Name the blood parasite species.
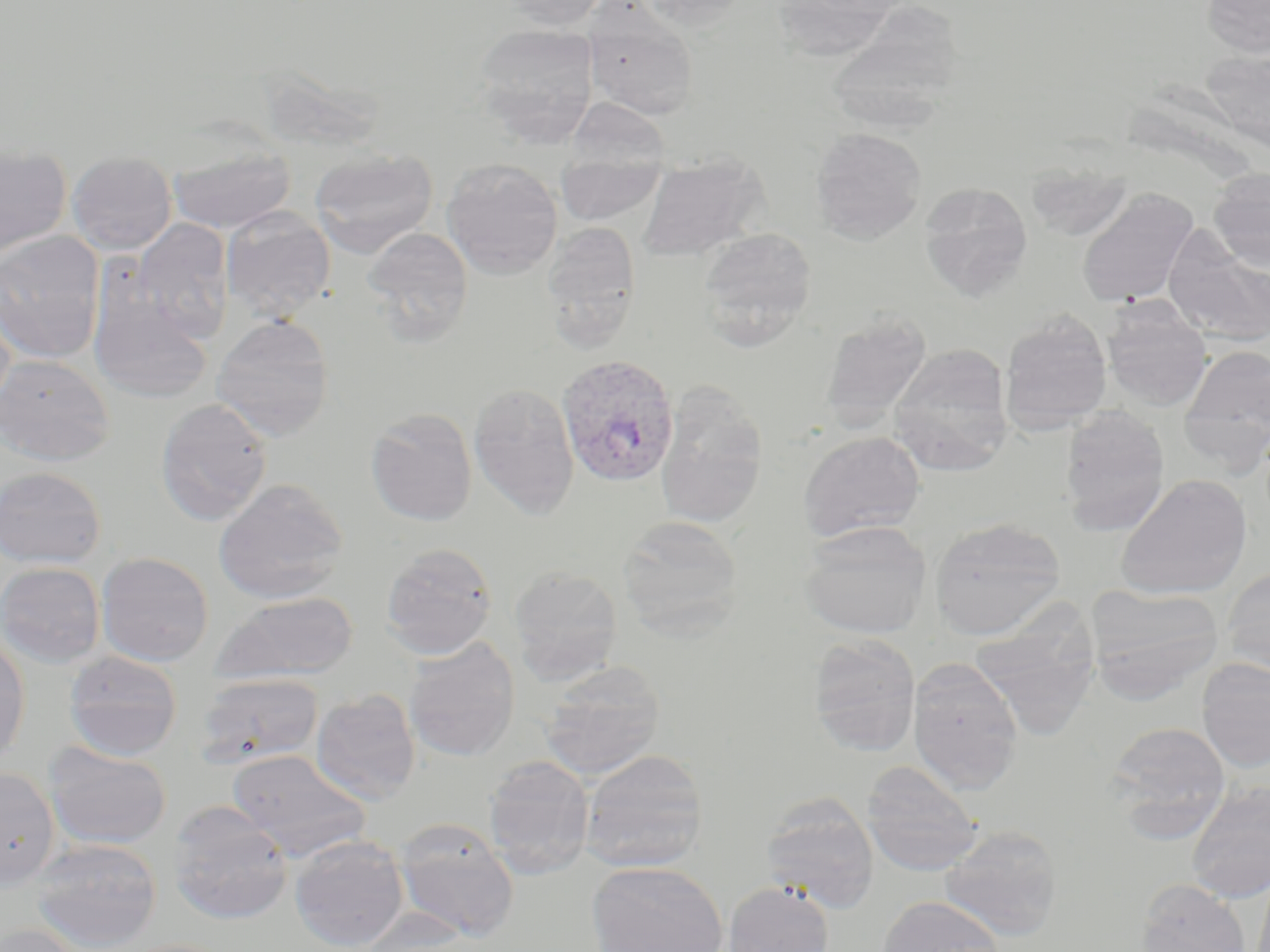
Plasmodium vivax.

Summary:
  - Coordinate format: approximate bounding boxes as (x1, y1, x2, y2) in pixels
  - Plasmodium vivax-infected red blood cell locations: (556, 354, 681, 488)
  - Uninfected red blood cell locations: (496, 0, 612, 30), (636, 0, 751, 29), (776, 0, 901, 63), (1200, 0, 1270, 58), (836, 2, 964, 138), (582, 5, 701, 121), (472, 22, 600, 146), (1200, 48, 1270, 153), (565, 97, 671, 172), (810, 127, 927, 244), (0, 142, 72, 260), (167, 144, 295, 233), (310, 147, 438, 257), (66, 151, 178, 255), (636, 153, 769, 263), (441, 157, 563, 279), (555, 159, 668, 226), (1025, 165, 1134, 241), (1208, 168, 1270, 273), (918, 182, 1034, 303), (1076, 188, 1200, 308), (221, 207, 336, 320), (132, 218, 234, 341), (541, 220, 642, 353), (1162, 226, 1270, 348), (361, 227, 473, 344), (696, 227, 817, 347), (0, 230, 105, 364), (87, 285, 213, 405), (1101, 298, 1213, 411), (0, 306, 15, 414), (819, 310, 932, 433), (999, 311, 1113, 434), (211, 314, 334, 441), (888, 344, 1014, 475), (1178, 345, 1270, 472), (0, 354, 114, 464), (468, 381, 580, 519), (654, 383, 769, 528), (155, 397, 273, 526), (1059, 405, 1171, 536), (365, 407, 478, 526), (797, 431, 926, 543), (0, 466, 107, 569), (1115, 473, 1253, 600), (213, 478, 348, 604), (617, 515, 743, 637), (928, 516, 1066, 641), (799, 520, 932, 639), (380, 542, 498, 659), (96, 551, 214, 666), (1, 561, 105, 668), (509, 565, 623, 684), (1221, 567, 1270, 677), (1085, 584, 1223, 703), (214, 592, 359, 684), (970, 608, 1100, 740), (0, 630, 30, 765), (807, 633, 921, 757), (403, 637, 520, 763), (63, 650, 183, 760), (907, 657, 1024, 794), (1196, 659, 1270, 773), (539, 661, 665, 780), (194, 673, 324, 768), (310, 689, 421, 806), (1106, 721, 1231, 836), (43, 742, 172, 849), (227, 749, 372, 861), (579, 749, 709, 873), (483, 755, 595, 879), (860, 760, 985, 877), (0, 766, 60, 889), (1185, 781, 1270, 903), (759, 793, 880, 913), (167, 801, 294, 925), (394, 820, 519, 941), (939, 824, 1063, 940), (289, 835, 409, 952), (30, 838, 163, 951), (587, 862, 728, 952), (1135, 878, 1251, 952), (723, 880, 834, 952), (878, 895, 1006, 952), (350, 908, 479, 952), (0, 924, 87, 952), (117, 938, 235, 952)
  - Preparation: thin blood smear
  - Modality: light microscopy
  - Image size: 1270×952 pixels
  - Magnification: 1000x
  - Field of view: single
  - Stain: May-Grünwald-Giemsa